Evaluate for malaria.
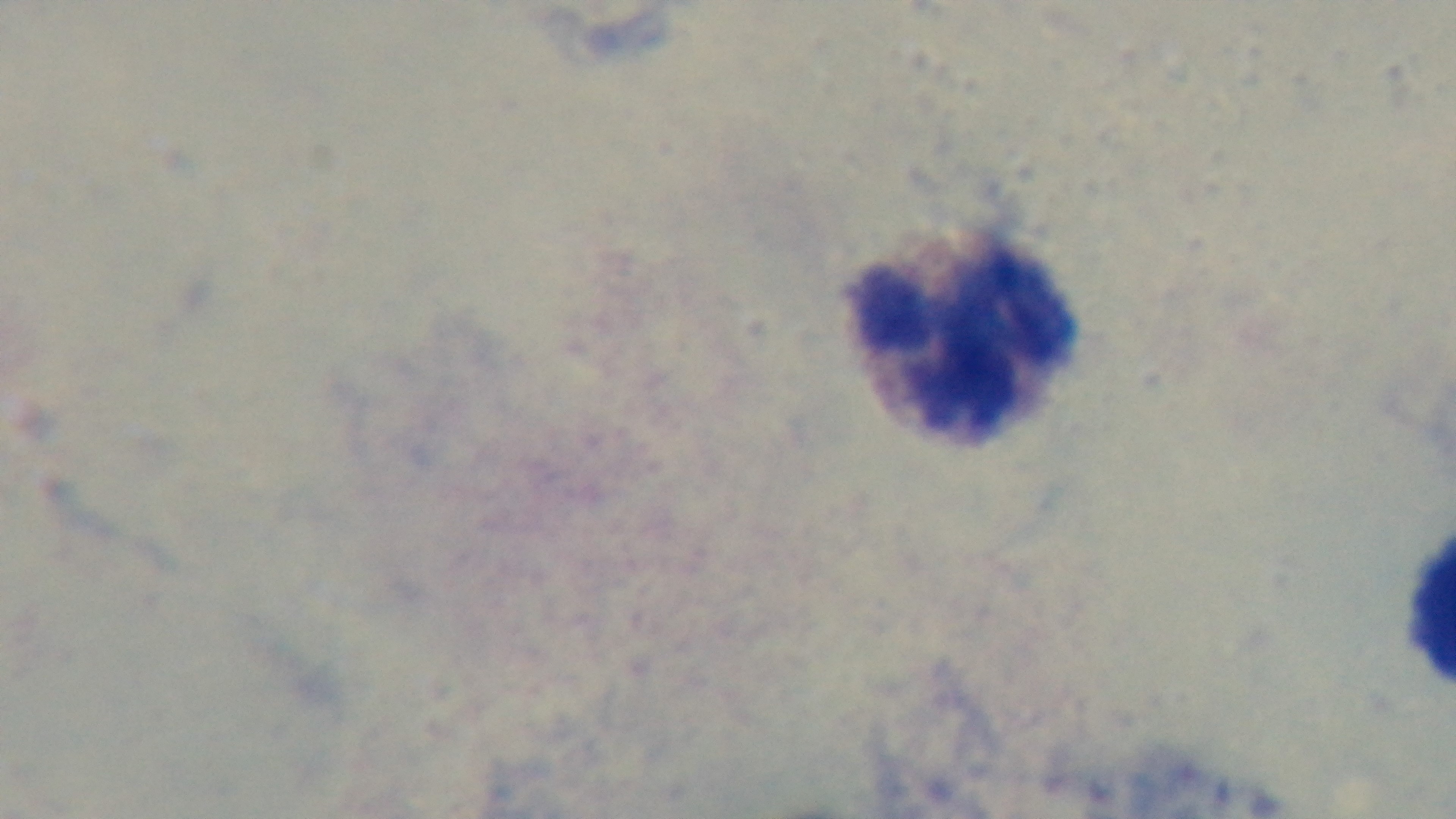
Uninfected.

Preparation: thick blood film. Mounted 4K digital camera. Giemsa-stained. 100x oil-immersion objective. Photomicrograph. One field from the slide.